Name the parasite shown.
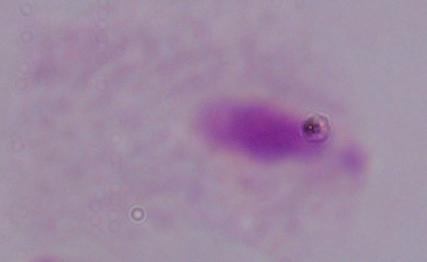
This is a trichomonad.

modality: photomicrograph
magnification: 1000x